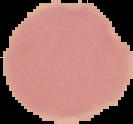
image_type: cell region segmented out of the field of view; surrounding area masked to black
preparation: thin blood film
image_size: 133×124 pixels
malaria_status: uninfected